Give the position of every Plasmodium falciparum parasite, noting its life-cycle stage.
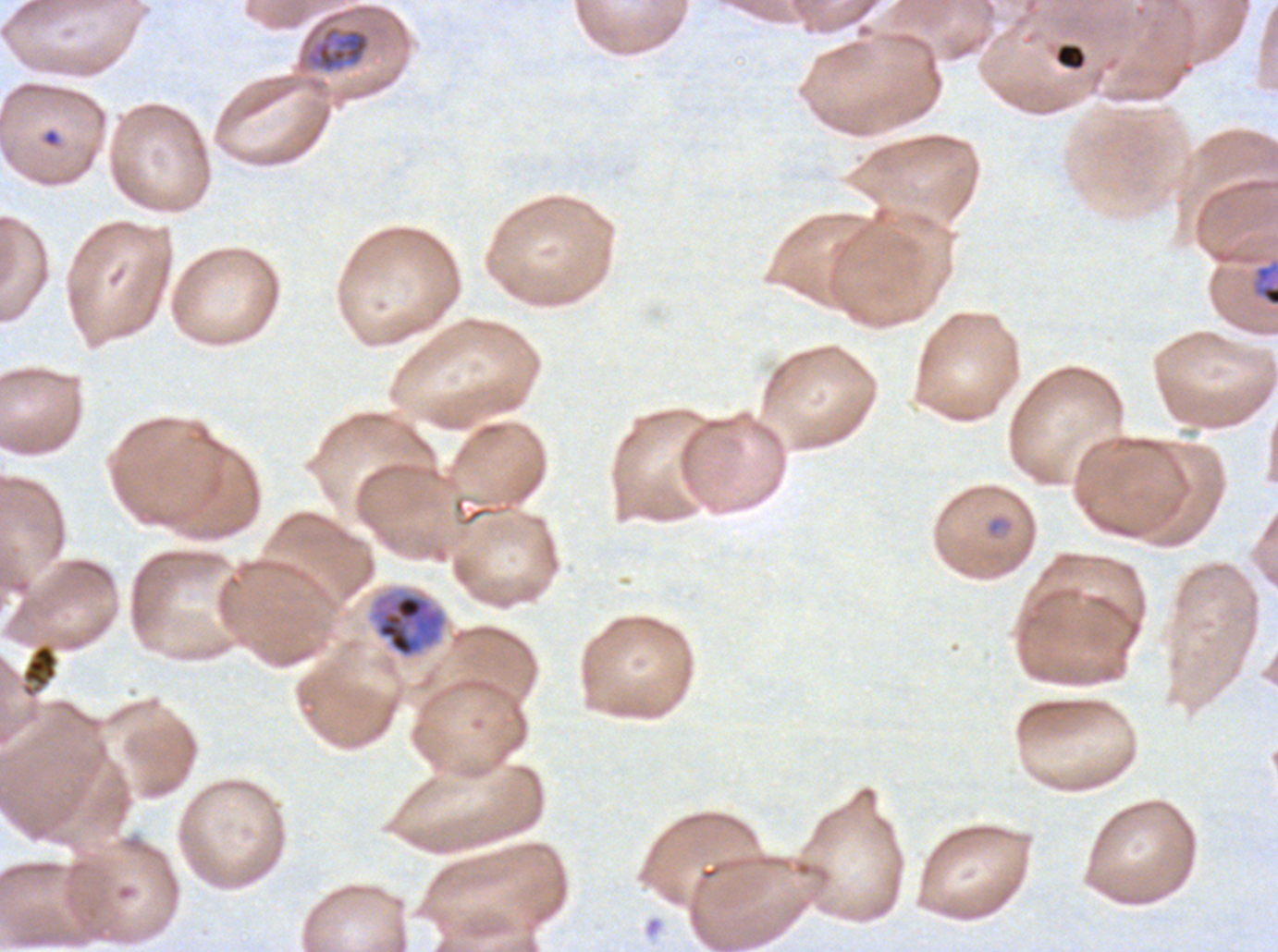

Approximate bounding rectangles given as corner coordinates in pixels from the top-left.
Rings: (x1=42, y1=128, x2=61, y2=147).
Late-ring/early-trophozoite forms: (x1=985, y1=514, x2=1014, y2=538).
Mid trophozoites: (x1=304, y1=24, x2=371, y2=73).
Late trophozoites: (x1=1252, y1=260, x2=1277, y2=308), (x1=370, y1=590, x2=447, y2=659).
No early schizonts, late schizonts, segmenters, or gametocytes observed.

Summary:
  - Debris locations: (x1=1056, y1=44, x2=1086, y2=68), (x1=21, y1=643, x2=58, y2=697)
  - Stain: Giemsa
  - Image size: 1278×952 pixels
  - Life-cycle stages observed: ring, late-ring/early-trophozoite, mid trophozoite, late trophozoite
  - Field of view: one sub-image of a larger composite
  - Preparation: thin blood smear
  - Specimen: Plasmodium falciparum from a patient in The Gambia, cultured ex vivo for 24 to 48 hours